Identify the blood parasite species.
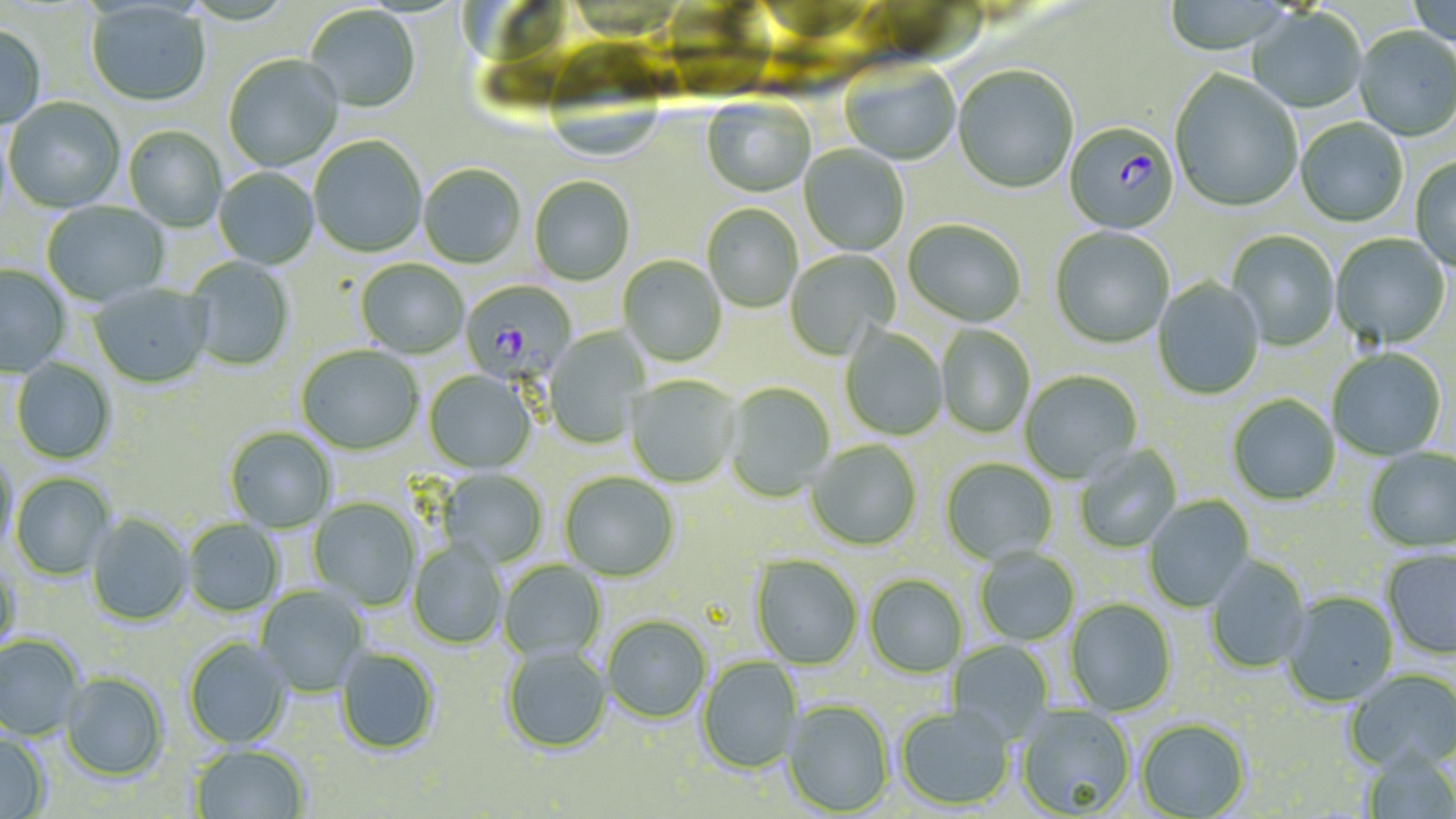
Plasmodium falciparum.

Approximate bounding boxes as (x1, y1, x2, y2) in pixels. Plasmodium falciparum-infected red blood cell locations: (1062, 123, 1180, 236), (460, 281, 576, 386). Uninfected red blood cell locations: (452, 0, 571, 69), (1161, 1, 1294, 57), (1406, 1, 1455, 49), (85, 3, 211, 109), (304, 6, 421, 114), (1246, 8, 1367, 114), (0, 26, 47, 130), (1353, 27, 1456, 143), (540, 41, 666, 157), (223, 55, 344, 172), (840, 62, 962, 166), (952, 66, 1079, 195), (1169, 71, 1303, 214), (701, 98, 815, 197), (3, 99, 126, 214), (1295, 119, 1408, 229), (123, 127, 228, 233), (308, 136, 427, 258), (799, 145, 910, 256), (1410, 157, 1456, 273), (419, 164, 525, 268), (214, 168, 319, 270), (529, 177, 635, 286), (41, 201, 169, 308), (701, 204, 803, 313), (902, 220, 1026, 328), (1049, 228, 1173, 349), (1227, 231, 1340, 352), (1331, 234, 1450, 349), (784, 249, 899, 360), (617, 255, 727, 367), (183, 257, 295, 371), (355, 260, 469, 360), (0, 266, 71, 378), (1152, 278, 1265, 400), (87, 283, 212, 388), (935, 325, 1035, 438), (839, 326, 947, 441), (544, 328, 649, 449), (296, 346, 423, 455), (1327, 349, 1446, 461), (10, 359, 116, 465), (424, 370, 536, 474), (1019, 371, 1142, 484), (625, 376, 742, 488), (723, 383, 836, 503), (1226, 394, 1340, 506), (224, 427, 336, 533), (807, 440, 922, 551), (1073, 444, 1182, 553), (1364, 448, 1456, 552), (0, 449, 18, 558), (940, 458, 1058, 565), (437, 468, 547, 568), (10, 472, 116, 580), (559, 472, 680, 582), (1143, 496, 1255, 612), (308, 497, 420, 609), (86, 514, 193, 627), (183, 519, 284, 617), (408, 541, 508, 650), (973, 547, 1080, 646), (1381, 548, 1456, 660), (749, 555, 862, 669), (1204, 555, 1311, 674), (0, 557, 23, 655), (498, 560, 606, 662), (864, 574, 967, 678), (255, 587, 369, 696), (1281, 591, 1399, 707), (1064, 598, 1176, 716), (602, 615, 711, 724), (0, 634, 84, 741), (184, 639, 292, 749), (946, 640, 1054, 743), (500, 645, 611, 753), (335, 648, 440, 755), (696, 657, 803, 773), (1343, 668, 1456, 772), (59, 672, 169, 782), (782, 699, 894, 816), (1015, 704, 1136, 817), (894, 705, 1014, 810), (1136, 718, 1250, 818), (0, 730, 50, 819), (189, 744, 309, 819), (1360, 745, 1456, 818). 1000x magnification. Thin blood smear. Image is 1456×819 pixels. One field of a larger specimen. May-Grünwald-Giemsa stain. Light microscopy.